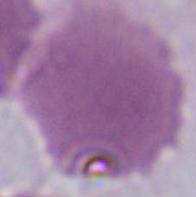
1000x magnification. Photomicrograph. An erythrocyte is seen.